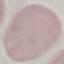
Result: no malaria parasites seen. Photographed with a smartphone camera at the microscope eyepiece. Automatically extracted cell patch, resized to 64 × 64 pixels. Giemsa stain. Thin smear of blood.